Identify the blood parasite species.
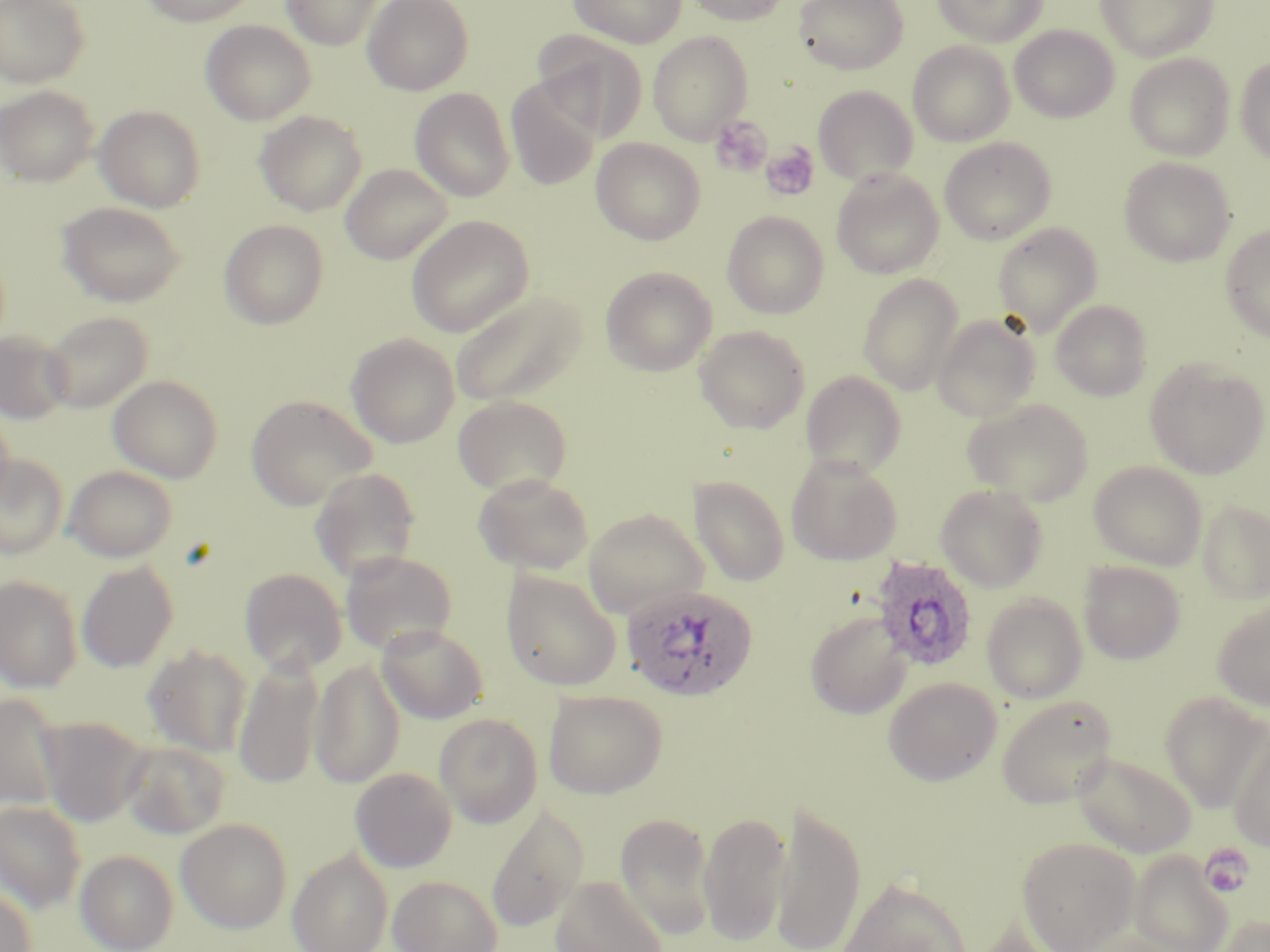
Plasmodium ovale.

Approximate bounding boxes as (x1, y1, x2, y2) in pixels. Uninfected red blood cell locations: (0, 0, 89, 88), (138, 0, 260, 26), (281, 0, 383, 50), (362, 0, 474, 95), (568, 0, 686, 48), (685, 0, 792, 26), (794, 0, 908, 74), (932, 0, 1047, 46), (1096, 0, 1219, 62), (200, 20, 316, 125), (1009, 24, 1118, 123), (532, 31, 648, 139), (648, 31, 754, 144), (908, 41, 1015, 147), (1125, 53, 1234, 160), (1235, 56, 1270, 164), (505, 78, 600, 191), (0, 85, 99, 186), (813, 85, 919, 185), (410, 88, 515, 202), (0, 97, 204, 195), (94, 104, 206, 212), (254, 110, 368, 216), (591, 137, 706, 245), (939, 137, 1056, 245), (1119, 156, 1235, 266), (340, 163, 453, 264), (831, 168, 944, 279), (57, 201, 187, 307), (722, 211, 829, 319), (406, 215, 534, 337), (219, 220, 329, 329), (992, 222, 1103, 336), (1220, 225, 1270, 342), (600, 266, 718, 376), (857, 273, 964, 395), (450, 289, 588, 408), (1050, 299, 1152, 400), (41, 311, 154, 413), (931, 313, 1041, 422), (695, 325, 810, 433), (0, 330, 72, 424), (346, 332, 460, 448), (1145, 358, 1269, 479), (801, 370, 907, 477), (108, 374, 223, 483), (245, 393, 377, 510), (453, 394, 572, 497), (961, 398, 1093, 505), (0, 403, 15, 510), (0, 454, 68, 559), (785, 454, 902, 565), (1089, 461, 1208, 569), (64, 465, 178, 562), (309, 466, 421, 583), (472, 472, 593, 574), (689, 472, 905, 580), (690, 476, 789, 586), (934, 483, 1049, 592), (1197, 499, 1270, 603), (582, 506, 710, 619), (340, 550, 458, 656), (76, 561, 179, 672), (1078, 561, 1186, 664), (239, 568, 347, 676), (501, 568, 622, 692), (0, 575, 83, 692), (981, 593, 1088, 704), (1212, 597, 1270, 711), (804, 610, 912, 719), (375, 623, 488, 724), (143, 644, 253, 757), (233, 655, 325, 789), (310, 658, 405, 789), (883, 677, 1002, 785), (543, 689, 667, 799), (0, 691, 64, 812), (1160, 692, 1270, 812), (996, 694, 1118, 808), (435, 712, 543, 827), (36, 716, 150, 827), (1227, 727, 1270, 853), (121, 740, 231, 839), (1072, 752, 1196, 858), (350, 767, 457, 873), (771, 799, 867, 952), (0, 801, 86, 914), (485, 804, 589, 933), (698, 809, 792, 946), (615, 812, 715, 941), (175, 818, 293, 934), (1017, 836, 1141, 952), (75, 849, 179, 952), (287, 849, 393, 952), (1129, 849, 1233, 952), (388, 875, 503, 952), (550, 875, 669, 952), (836, 877, 974, 951), (0, 886, 37, 952), (1209, 912, 1270, 952), (963, 917, 1073, 952). Plasmodium ovale-infected red blood cell locations: (869, 555, 979, 672), (619, 583, 759, 701). Platelet locations: (710, 116, 772, 177), (761, 142, 820, 201), (1201, 845, 1253, 898). Light microscopy. May-Grünwald-Giemsa stain. Thin blood smear. Captured at 1000x magnification. One field of a larger specimen. Image is 1270×952 pixels.